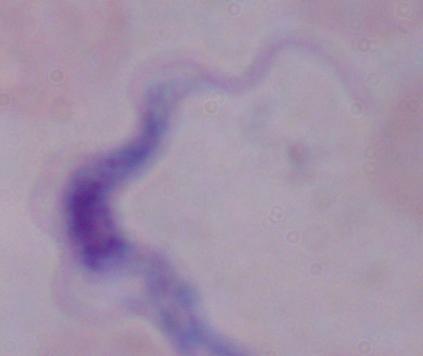
Captured at 1000x magnification. A trypanosome is seen. Photomicrograph.